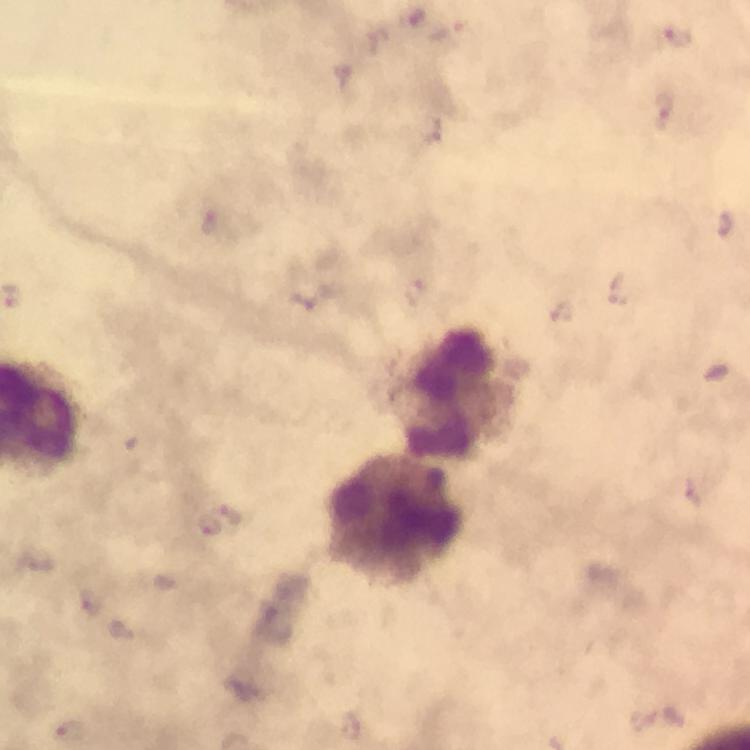

Approximate centers as [x, y] in pixels. Malaria parasite locations: [664, 110], [212, 223], [617, 290], [415, 295], [306, 298], [230, 514], [210, 529], [92, 605], [353, 727], [70, 732]. Leukocyte locations: [450, 391], [395, 519]. 100x magnification. A crop from one field of view. Giemsa-stained preparation. Smartphone photograph taken through a microscope. Image is 750×750 pixels. Thick smear. Immersion oil was used. From a malaria diagnostic workup.